Report the malaria status of this cell.
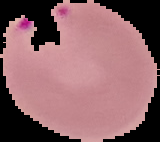

It is parasitized.

Image is 160×142 pixels. The area outside the segmented cell region is set to black. From a thin blood smear.